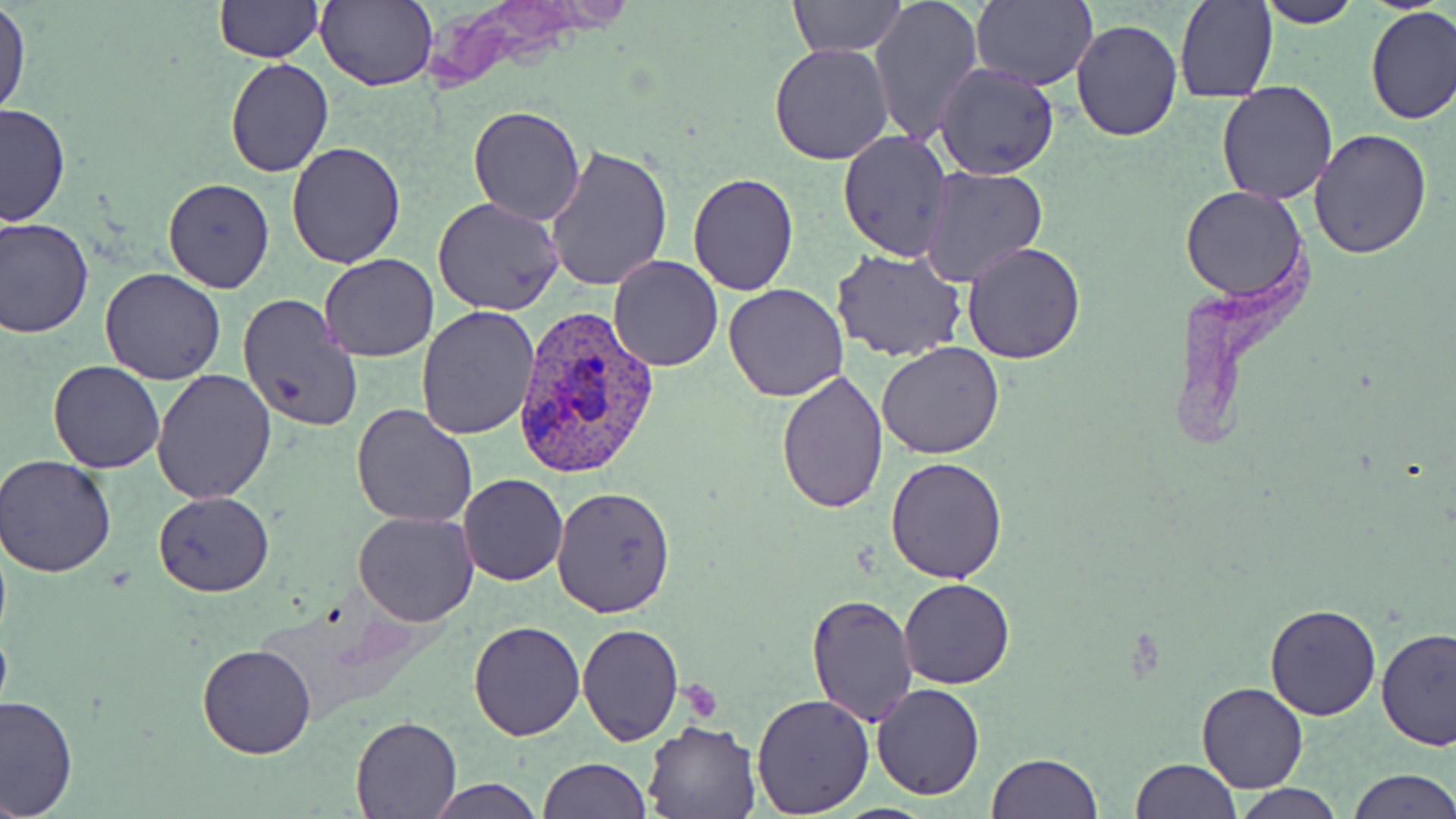

Approximate bounding boxes as (x1, y1, x2, y2) in pixels. Platelet locations: (679, 676, 721, 717). Uninfected red blood cell locations: (214, 0, 323, 62), (316, 0, 437, 91), (787, 0, 907, 58), (869, 0, 983, 147), (969, 1, 1098, 89), (1174, 1, 1276, 103), (1255, 1, 1364, 27), (0, 5, 30, 118), (1364, 6, 1455, 126), (1071, 18, 1184, 142), (769, 43, 894, 165), (225, 57, 333, 178), (934, 63, 1060, 181), (1216, 80, 1340, 205), (0, 104, 71, 229), (468, 104, 585, 225), (1310, 129, 1431, 259), (838, 131, 954, 259), (285, 141, 409, 267), (546, 145, 674, 291), (919, 165, 1047, 286), (687, 173, 798, 293), (164, 178, 275, 292), (1180, 185, 1307, 301), (434, 196, 565, 314), (0, 215, 95, 339), (962, 243, 1084, 365), (831, 248, 966, 363), (318, 252, 438, 361), (608, 255, 724, 371), (100, 268, 227, 385), (724, 283, 850, 401), (238, 293, 366, 434), (417, 306, 540, 440), (877, 341, 1003, 459), (48, 360, 163, 473), (775, 368, 887, 513), (149, 369, 276, 505), (17, 373, 145, 572), (351, 404, 478, 529), (0, 454, 116, 578), (886, 455, 1008, 582), (459, 474, 568, 585), (551, 483, 675, 617), (154, 492, 274, 596), (352, 510, 479, 627), (900, 578, 1015, 689), (805, 592, 918, 726), (1264, 602, 1382, 720), (468, 619, 585, 742), (577, 624, 683, 745), (1374, 628, 1456, 751), (198, 641, 316, 759), (870, 682, 986, 800), (1196, 683, 1308, 793), (751, 693, 874, 816), (0, 695, 77, 818), (351, 715, 461, 817), (642, 718, 764, 818), (987, 752, 1103, 819), (539, 757, 650, 819), (1131, 759, 1240, 818), (1348, 769, 1456, 819), (427, 778, 544, 818), (1230, 783, 1345, 819). Plasmodium vivax-infected red blood cell locations: (509, 304, 662, 482). Slide-level diagnosis: Plasmodium vivax. 1000x magnification. Thin blood smear. Image is 1456×819 pixels. May-Grünwald-Giemsa-stained preparation. Optical microscopy. One field of a larger specimen.